Report the malaria status of this cell.
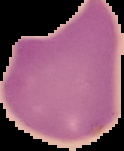

Uninfected.

image_type: segmented cell region with the area outside set to black
image_size: 124×151 pixels
preparation: thin blood smear